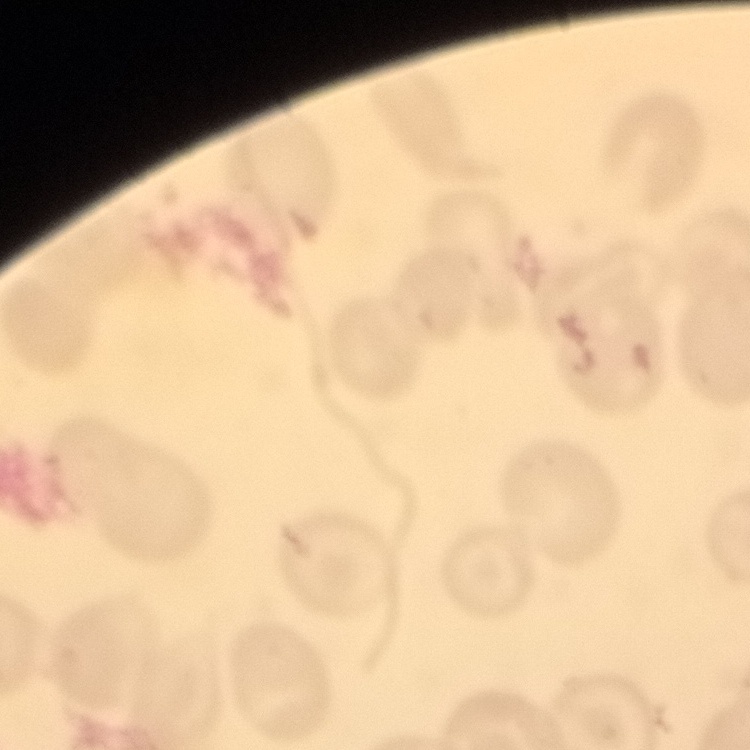
Summary:
  - Erythrocyte morphology: no rouleaux formation
  - Preparation: thin peripheral smear
  - Stain: Field's or Giemsa
  - Image type: one tile cut from a larger photomicrograph